Name the parasite shown.
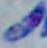

Toxoplasma gondii.

magnification = 1000x
modality = photomicrograph